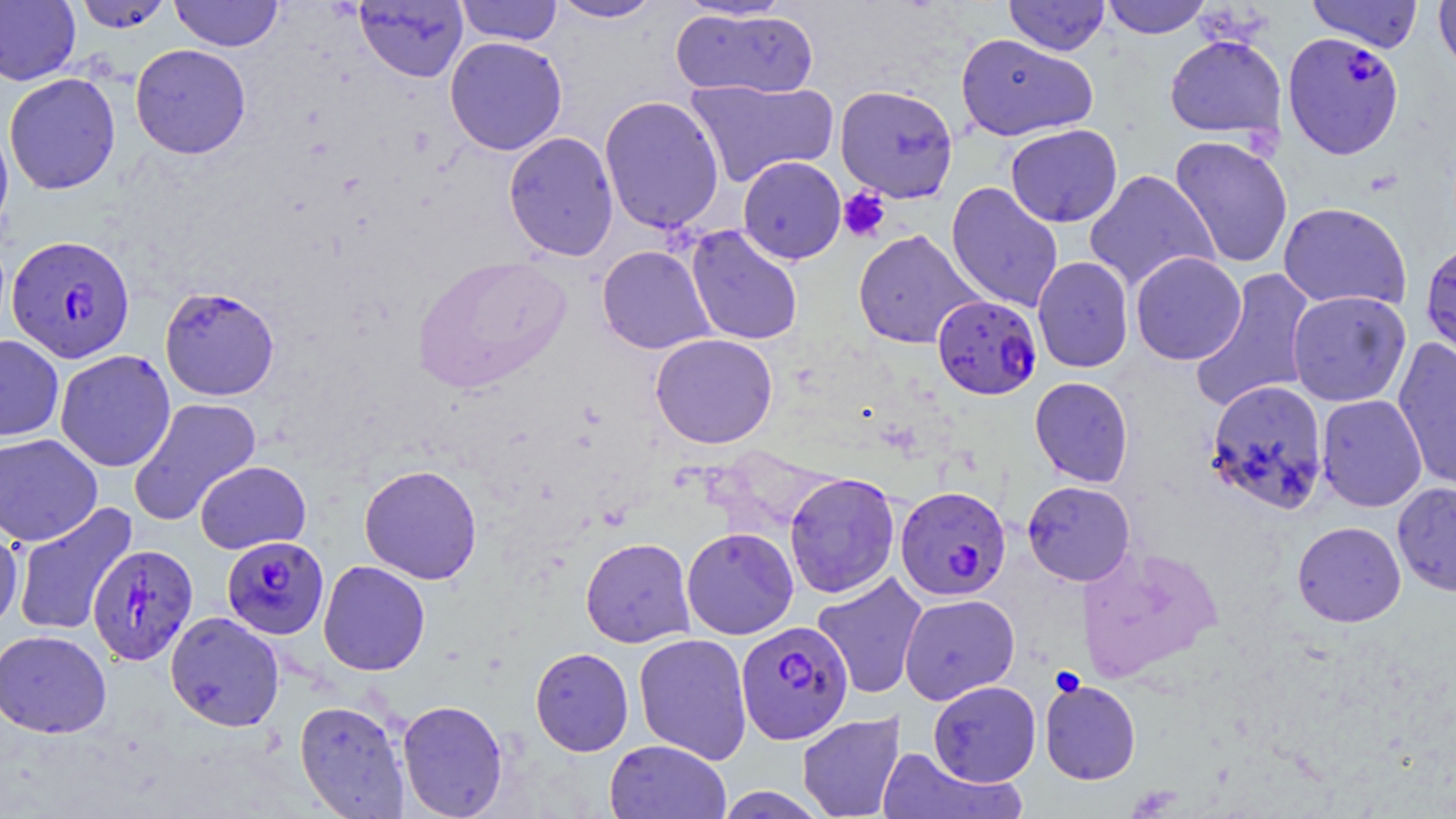
slide_level_diagnosis: Plasmodium falciparum
field_of_view: single
stain: May-Grünwald-Giemsa
preparation: thin blood smear
magnification: 1000x
uninfected_red_blood_cell_locations: 'approximate bounding boxes as named x1/y1/x2/y2 corners in pixels: (x1=0, y1=0, x2=80, y2=85), (x1=73, y1=0, x2=174, y2=33), (x1=170, y1=0, x2=283, y2=51), (x1=354, y1=0, x2=468, y2=83), (x1=454, y1=0, x2=563, y2=46), (x1=548, y1=0, x2=664, y2=23), (x1=670, y1=0, x2=800, y2=21), (x1=1004, y1=0, x2=1110, y2=55), (x1=1101, y1=0, x2=1212, y2=38), (x1=1306, y1=0, x2=1424, y2=52), (x1=1433, y1=0, x2=1456, y2=80), (x1=670, y1=7, x2=818, y2=100), (x1=955, y1=33, x2=1098, y2=141), (x1=1164, y1=34, x2=1287, y2=140), (x1=444, y1=36, x2=567, y2=156), (x1=130, y1=44, x2=252, y2=159), (x1=4, y1=72, x2=121, y2=195), (x1=684, y1=78, x2=838, y2=188), (x1=835, y1=84, x2=959, y2=203), (x1=599, y1=95, x2=725, y2=235), (x1=0, y1=115, x2=14, y2=243), (x1=1005, y1=124, x2=1123, y2=227), (x1=503, y1=131, x2=619, y2=261), (x1=1169, y1=135, x2=1294, y2=269), (x1=737, y1=156, x2=847, y2=264), (x1=1083, y1=170, x2=1219, y2=293), (x1=946, y1=182, x2=1063, y2=312), (x1=1278, y1=202, x2=1411, y2=311), (x1=685, y1=225, x2=804, y2=346), (x1=852, y1=229, x2=983, y2=349), (x1=1420, y1=240, x2=1456, y2=365), (x1=596, y1=245, x2=717, y2=354), (x1=1130, y1=251, x2=1246, y2=365), (x1=413, y1=256, x2=572, y2=392), (x1=1032, y1=257, x2=1134, y2=373), (x1=1190, y1=269, x2=1317, y2=411), (x1=159, y1=285, x2=280, y2=401), (x1=1287, y1=290, x2=1411, y2=407), (x1=650, y1=333, x2=779, y2=449), (x1=0, y1=334, x2=64, y2=441), (x1=1392, y1=336, x2=1456, y2=493), (x1=55, y1=350, x2=176, y2=472), (x1=1029, y1=376, x2=1134, y2=488), (x1=1204, y1=379, x2=1329, y2=515), (x1=1316, y1=394, x2=1428, y2=512), (x1=128, y1=397, x2=262, y2=526), (x1=0, y1=433, x2=103, y2=546), (x1=194, y1=461, x2=311, y2=554), (x1=359, y1=464, x2=483, y2=584), (x1=784, y1=472, x2=900, y2=599), (x1=1021, y1=480, x2=1136, y2=586), (x1=1392, y1=481, x2=1456, y2=596), (x1=11, y1=502, x2=138, y2=638), (x1=0, y1=521, x2=22, y2=636), (x1=1292, y1=521, x2=1406, y2=627), (x1=681, y1=527, x2=799, y2=639), (x1=580, y1=537, x2=695, y2=648), (x1=1076, y1=544, x2=1224, y2=683), (x1=318, y1=560, x2=431, y2=676), (x1=811, y1=571, x2=928, y2=699), (x1=899, y1=593, x2=1020, y2=704), (x1=165, y1=611, x2=285, y2=731), (x1=0, y1=629, x2=112, y2=738), (x1=633, y1=632, x2=752, y2=764), (x1=530, y1=647, x2=634, y2=756), (x1=1039, y1=679, x2=1141, y2=785), (x1=928, y1=680, x2=1041, y2=787), (x1=397, y1=699, x2=508, y2=818), (x1=294, y1=700, x2=410, y2=817), (x1=796, y1=712, x2=906, y2=819), (x1=604, y1=740, x2=731, y2=818), (x1=875, y1=747, x2=1024, y2=819), (x1=713, y1=787, x2=828, y2=818)'
platelet_locations: 'approximate bounding boxes as named x1/y1/x2/y2 corners in pixels: (x1=837, y1=188, x2=891, y2=242)'
image_size: 1456×819 pixels
modality: optical microscopy
plasmodium_falciparum_infected_red_blood_cell_locations: 'approximate bounding boxes as named x1/y1/x2/y2 corners in pixels: (x1=1283, y1=32, x2=1404, y2=159), (x1=6, y1=234, x2=136, y2=363), (x1=932, y1=295, x2=1042, y2=400), (x1=894, y1=485, x2=1012, y2=601), (x1=221, y1=535, x2=329, y2=639), (x1=87, y1=544, x2=198, y2=665), (x1=736, y1=620, x2=854, y2=744)'